Locate and identify every blood parasite.
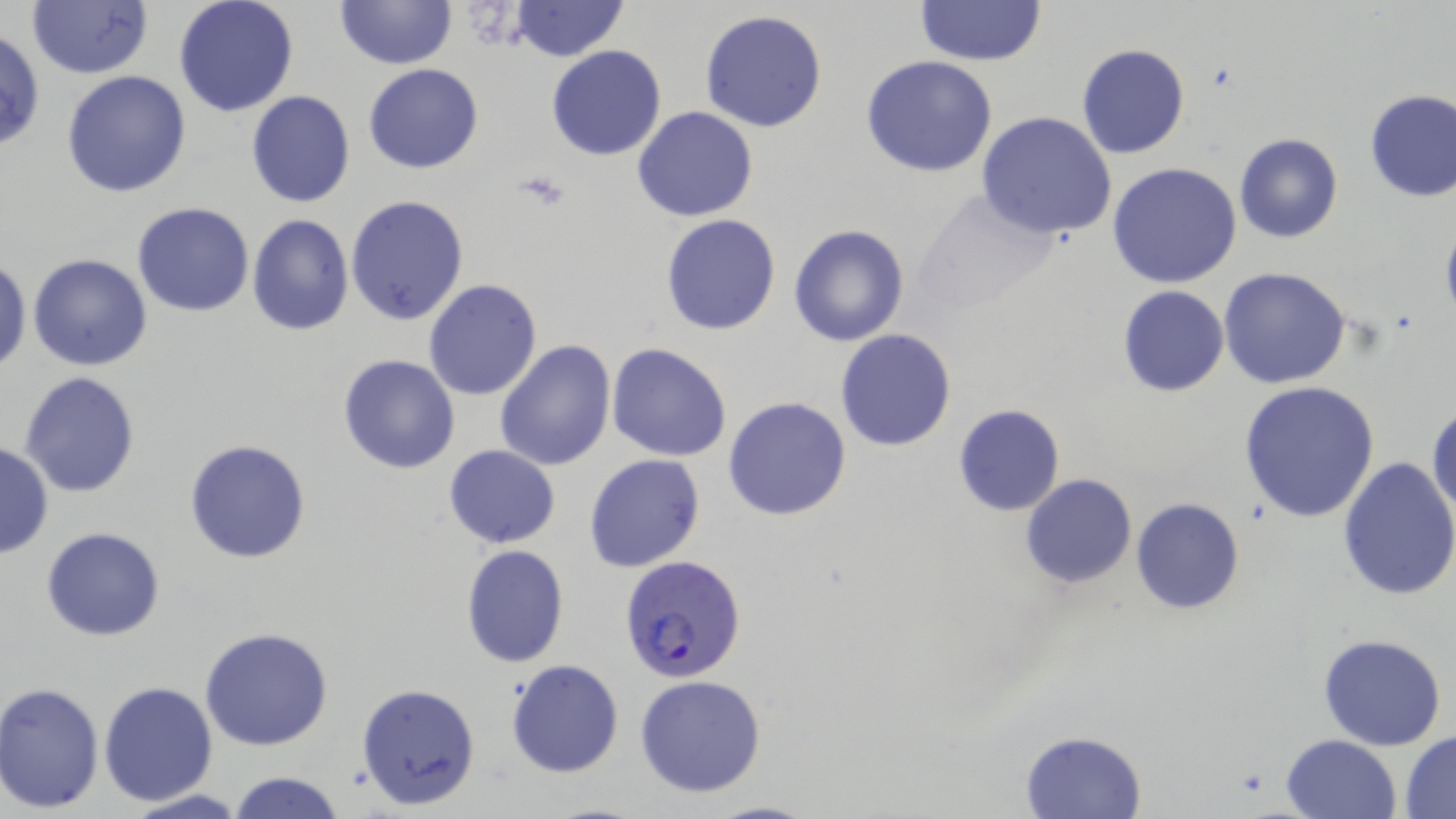
Approximate bounding boxes as (x1, y1, x2, y2) in pixels.
Plasmodium falciparum-infected red blood cells: (619, 556, 749, 683).
No Plasmodium ovale, Plasmodium malariae, Plasmodium vivax, Babesia divergens, or Trypanosoma brucei observed.

Platelet locations: (516, 169, 569, 211). Uninfected red blood cell locations: (173, 0, 300, 118), (334, 0, 458, 69), (914, 0, 1046, 66), (511, 1, 627, 62), (26, 2, 152, 79), (699, 9, 828, 133), (1076, 43, 1189, 159), (546, 44, 667, 162), (860, 55, 998, 177), (362, 63, 484, 174), (62, 70, 192, 196), (1362, 88, 1455, 202), (246, 90, 355, 208), (632, 106, 759, 222), (976, 112, 1118, 241), (1233, 134, 1343, 242), (1108, 162, 1243, 288), (912, 188, 1065, 317), (347, 194, 469, 325), (132, 202, 254, 316), (247, 214, 353, 335), (661, 214, 783, 335), (1439, 217, 1456, 333), (789, 224, 910, 346), (28, 253, 153, 372), (0, 258, 28, 372), (1219, 268, 1350, 388), (424, 279, 543, 401), (1118, 286, 1229, 397), (835, 328, 957, 452), (495, 339, 616, 469), (607, 343, 731, 461), (337, 354, 461, 474), (17, 371, 142, 498), (1239, 380, 1381, 522), (723, 396, 852, 521), (1427, 400, 1456, 521), (952, 404, 1066, 516), (184, 438, 312, 563), (0, 442, 54, 557), (443, 445, 561, 548), (584, 452, 705, 572), (1336, 456, 1456, 600), (1020, 473, 1136, 588), (1131, 497, 1244, 615), (41, 527, 165, 641), (460, 544, 570, 668), (199, 626, 333, 750), (1317, 634, 1448, 751), (507, 658, 623, 778), (634, 674, 767, 796), (0, 681, 105, 813), (98, 681, 218, 805), (358, 681, 482, 810), (1020, 730, 1146, 818), (1401, 731, 1456, 815), (1281, 735, 1402, 819), (228, 771, 347, 819), (120, 790, 247, 819), (702, 798, 819, 818). Slide-level diagnosis: Plasmodium falciparum. May-Grünwald-Giemsa-stained preparation. One field of a larger specimen. Image is 1456×819 pixels. Thin blood smear. Optical microscopy. Captured at 1000x magnification.